Outline each blood parasite and name the species.
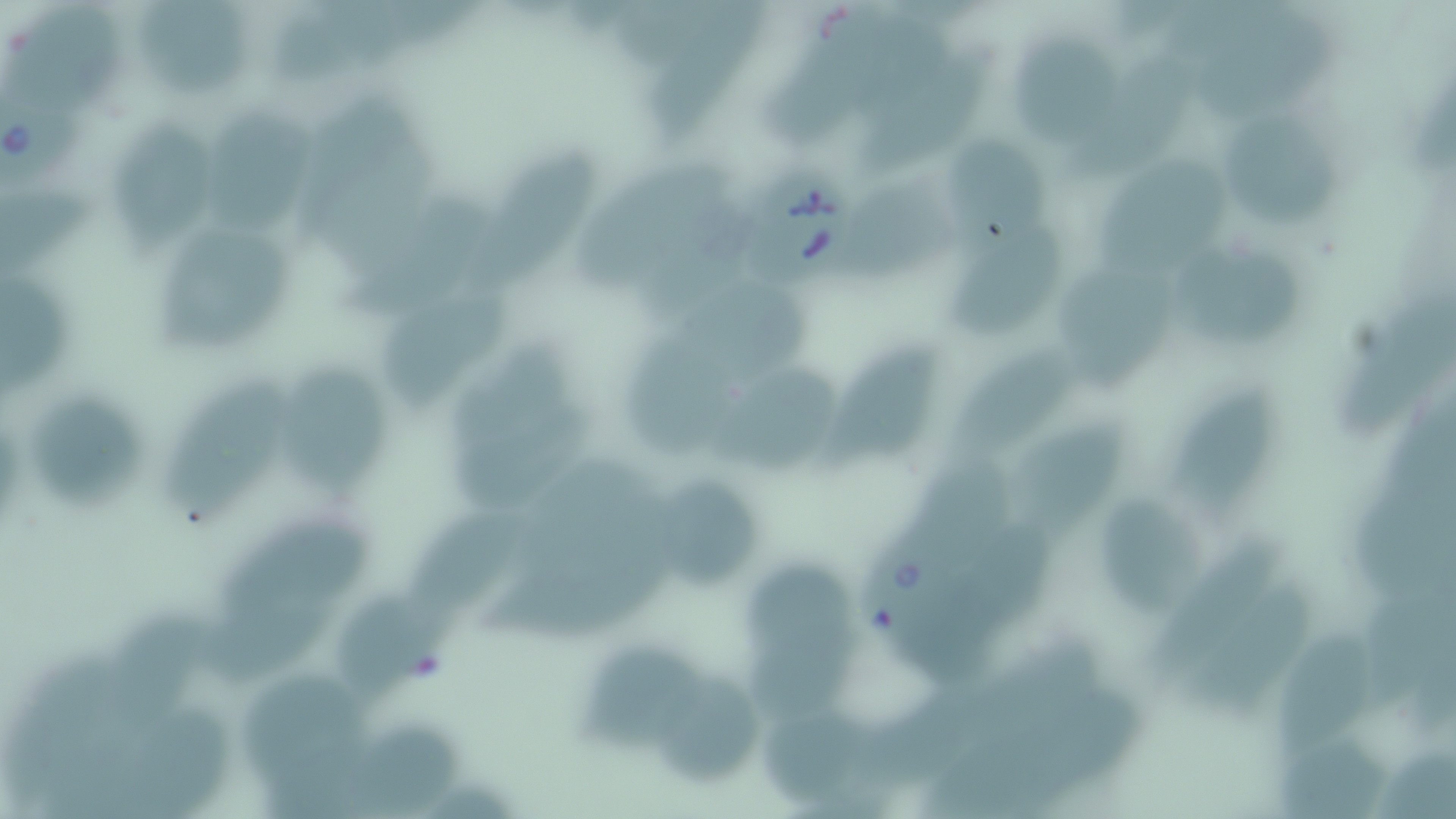
Approximate bounding boxes as (x1, y1, x2, y2) in pixels.
Babesia divergens-infected red blood cells: (0, 99, 88, 192), (743, 169, 862, 288), (856, 533, 987, 659).
No Plasmodium falciparum, Plasmodium ovale, Plasmodium malariae, Plasmodium vivax, or Trypanosoma brucei observed.

Uninfected red blood cell locations: (6, 0, 123, 107), (137, 1, 249, 102), (647, 1, 759, 140), (768, 3, 921, 148), (1192, 14, 1344, 117), (1001, 33, 1128, 147), (863, 55, 1001, 182), (207, 107, 311, 240), (1225, 119, 1341, 237), (110, 122, 220, 252), (937, 132, 1055, 257), (469, 142, 594, 293), (1091, 154, 1235, 282), (580, 161, 730, 289), (852, 190, 969, 285), (349, 195, 493, 311), (948, 224, 1064, 340), (161, 225, 294, 354), (1169, 246, 1310, 347), (680, 268, 811, 383), (1064, 270, 1188, 386), (2, 272, 71, 406), (383, 279, 515, 413), (1343, 291, 1451, 442), (622, 332, 736, 462), (821, 336, 940, 472), (456, 343, 577, 454), (952, 349, 1107, 458), (709, 358, 840, 476), (283, 364, 386, 499), (159, 373, 295, 522), (17, 384, 155, 515), (1165, 384, 1285, 509), (451, 403, 596, 506), (1009, 421, 1129, 535), (904, 452, 1018, 561), (658, 471, 763, 593), (1088, 481, 1214, 620), (406, 503, 534, 621), (219, 512, 375, 611), (743, 561, 861, 675), (210, 581, 351, 679), (1194, 582, 1319, 725), (341, 594, 467, 696), (101, 612, 205, 733), (1274, 625, 1377, 753), (585, 644, 713, 752), (233, 668, 377, 801), (656, 672, 762, 793), (762, 712, 874, 804), (350, 726, 467, 814). Slide-level diagnosis: Babesia divergens. Image is 1456×819 pixels. 1000x magnification. May-Grünwald-Giemsa stain. Thin blood film. One field of a larger specimen. Optical microscopy.